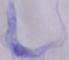

Summary:
  - Modality: photomicrograph
  - Magnification: 1000x
  - Identification: trypanosome